Locate every leukocyte (white blood cell).
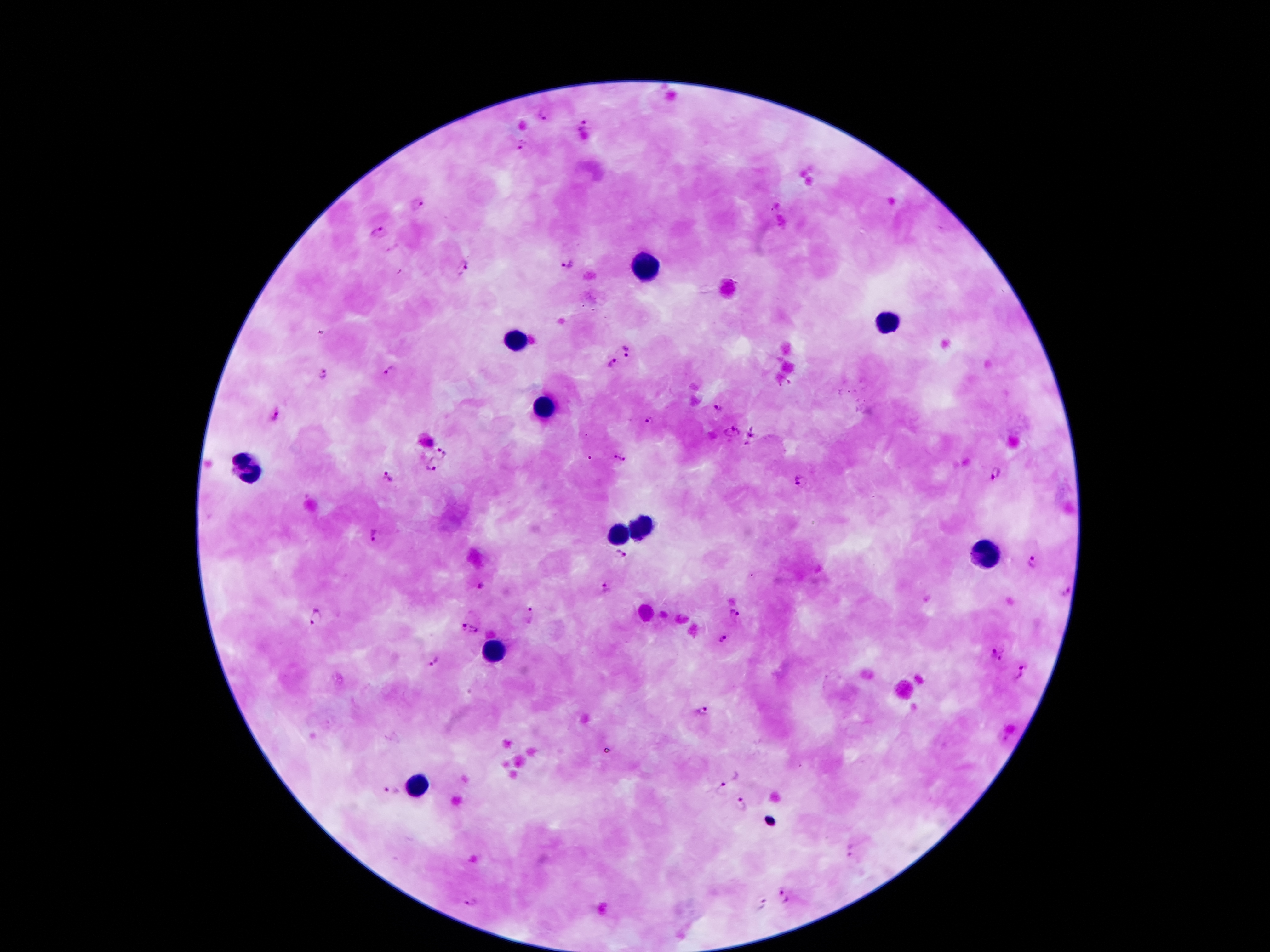
Approximate centers as {x, y} in pixels.
Leukocytes: {644, 264}, {890, 323}, {516, 338}, {542, 409}, {246, 472}, {639, 529}, {615, 536}, {984, 554}, {493, 651}, {414, 784}.

Plasmodium parasite locations: {543, 114}, {586, 123}, {521, 145}, {419, 204}, {383, 232}, {567, 266}, {462, 269}, {627, 352}, {612, 363}, {392, 371}, {323, 374}, {719, 406}, {275, 415}, {649, 421}, {733, 432}, {431, 444}, {445, 451}, {619, 459}, {435, 465}, {995, 473}, {390, 476}, {800, 480}, {371, 534}, {622, 555}, {1032, 563}, {481, 586}, {606, 587}, {1065, 592}, {317, 615}, {532, 615}, {735, 616}, {464, 626}, {475, 631}, {722, 639}, {997, 654}, {432, 662}, {1021, 673}, {704, 712}, {728, 775}, {392, 792}, {743, 804}, {852, 850}, {784, 897}, {472, 904}, {760, 904}. Giemsa-stained preparation. Thick blood smear. One field from this slide. Image is 1270×952 pixels. 100x magnification. Patient malaria status: infected with Plasmodium falciparum. Smartphone photograph taken through the microscope eyepiece.